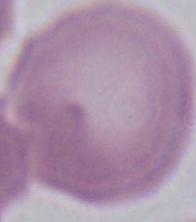

identification: red blood cell
modality: micrograph
magnification: 1000x